Locate leukocytes (white blood cells).
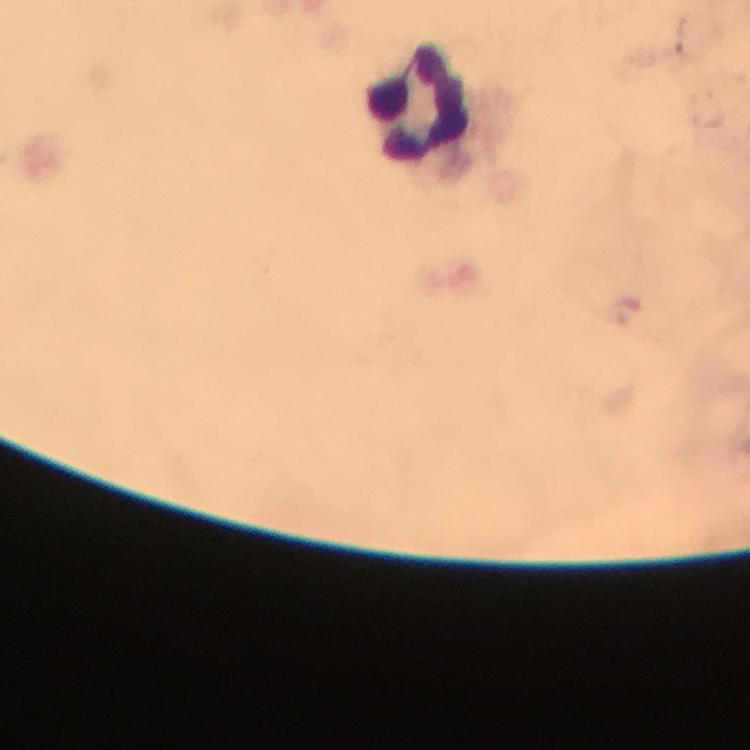
Approximate centers as [x, y] in pixels.
Leukocytes: [418, 104].

Summary:
  - Plasmodium parasites: none seen
  - Image size: 750×750 pixels
  - Preparation: thick smear
  - Magnification: 100x
  - Immersion oil: applied
  - Capture: smartphone mounted on the microscope
  - Stain: Giemsa
  - Cropped from: a single field of view
  - Context: from a diagnostic examination for malaria